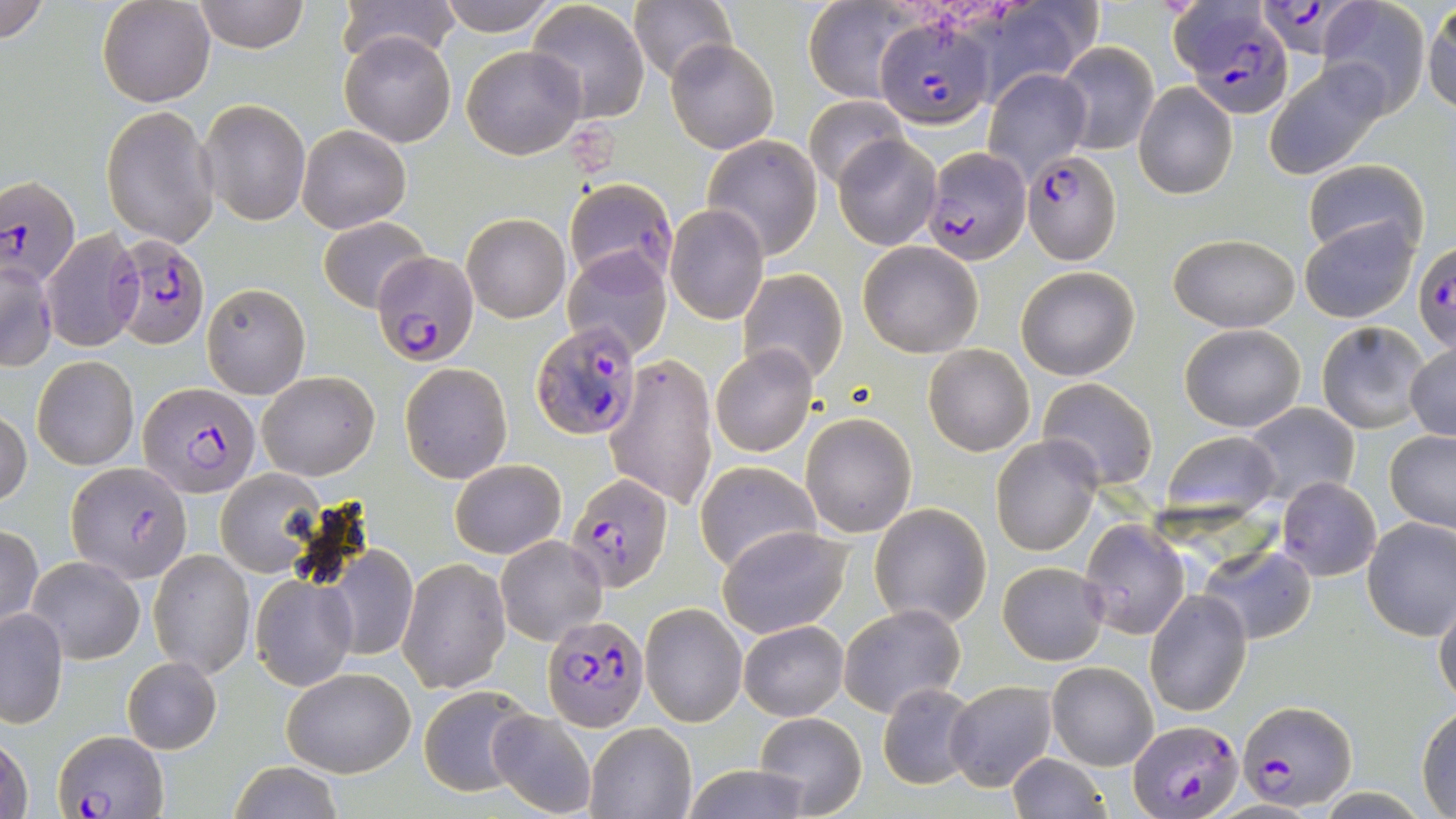

Approximate bounding boxes as (x1,y1)-(x2,y2) corner pairs in pixels. Plasmodium falciparum-infected red blood cell locations: (1259,0)-(1386,65), (1170,2)-(1294,116), (875,16)-(996,129), (921,146)-(1031,265), (1021,149)-(1120,262), (0,176)-(78,287), (108,232)-(209,349), (1413,243)-(1456,356), (374,251)-(479,366), (532,322)-(643,443), (136,382)-(261,495), (68,462)-(191,583), (564,472)-(672,593), (541,615)-(649,730), (1237,700)-(1357,809), (1128,719)-(1244,818), (56,730)-(168,817). Uninfected red blood cell locations: (0,0)-(52,45), (97,0)-(214,106), (193,0)-(309,52), (333,0)-(461,64), (434,0)-(563,34), (629,0)-(738,85), (802,0)-(917,103), (526,1)-(650,123), (1317,1)-(1432,115), (1424,1)-(1456,117), (340,31)-(456,146), (666,38)-(778,154), (1057,40)-(1157,156), (461,45)-(587,159), (1263,61)-(1394,178), (984,67)-(1092,180), (1133,82)-(1237,199), (804,94)-(908,190), (199,98)-(310,226), (102,106)-(218,248), (296,123)-(412,233), (833,133)-(941,250), (702,136)-(822,260), (1304,160)-(1428,260), (562,178)-(678,288), (665,204)-(769,324), (462,212)-(570,322), (1299,214)-(1418,322), (318,217)-(430,312), (41,229)-(142,351), (1168,234)-(1300,332), (857,241)-(983,356), (562,248)-(672,360), (1,258)-(56,371), (1015,266)-(1140,380), (738,268)-(847,385), (201,282)-(311,399), (1316,320)-(1429,434), (1180,322)-(1306,432), (922,343)-(1036,457), (711,344)-(818,458), (1405,344)-(1456,442), (605,351)-(718,511), (32,355)-(138,470), (400,362)-(512,484), (258,370)-(380,479), (1038,377)-(1159,488), (1243,402)-(1361,510), (0,410)-(31,508), (802,413)-(917,538), (1384,430)-(1456,532), (1160,431)-(1282,525), (990,435)-(1100,556), (450,459)-(566,559), (694,462)-(822,574), (216,471)-(321,577), (1277,477)-(1382,582), (868,502)-(993,629), (1361,517)-(1456,640), (1079,520)-(1191,640), (0,525)-(43,633), (718,526)-(852,638), (496,536)-(605,644), (323,540)-(419,662), (1197,542)-(1317,644), (150,549)-(254,677), (27,556)-(145,665), (399,557)-(511,693), (997,561)-(1109,666), (250,573)-(357,690), (1142,588)-(1252,717), (1434,597)-(1456,708), (838,602)-(965,717), (641,603)-(747,727), (1,608)-(68,727), (739,620)-(849,720), (120,656)-(221,754), (1046,661)-(1158,769), (281,667)-(416,777), (944,681)-(1058,791), (877,683)-(979,789), (418,685)-(540,797), (1416,705)-(1456,815), (487,709)-(598,819), (755,709)-(866,817), (585,724)-(696,818), (1,730)-(34,819), (1007,753)-(1110,819), (227,762)-(345,819), (678,763)-(818,819). Slide-level diagnosis: Plasmodium falciparum. Optical microscopy. Captured at 1000x magnification. Single field of view. Image is 1456×819 pixels. Thin blood smear. May-Grünwald-Giemsa-stained preparation.